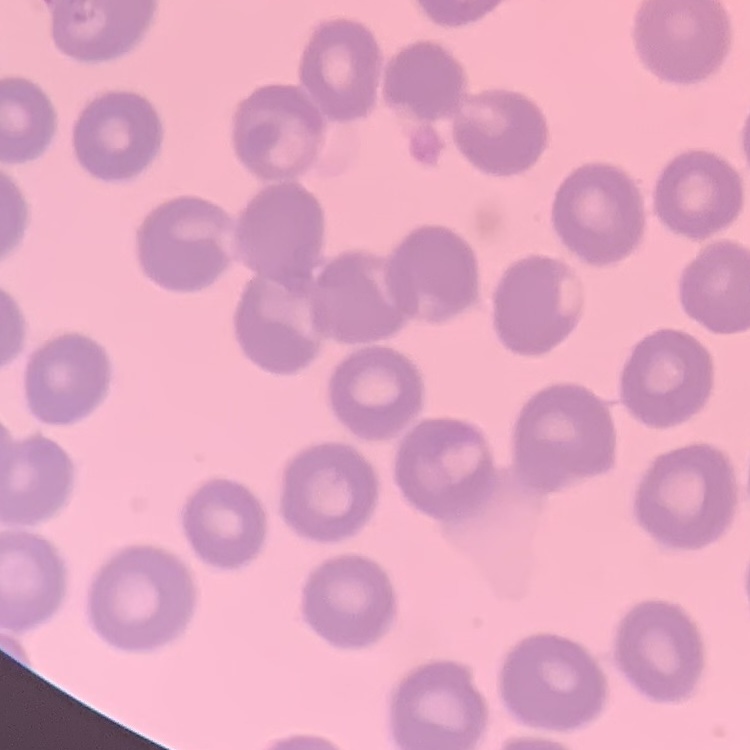
Summary:
  - Red blood cell morphology: no rouleaux formation
  - Image type: one tile cut from a larger photomicrograph
  - Preparation: thin blood smear
  - Stain: Field's or Giemsa